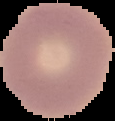

{
  "preparation": "thin blood smear",
  "image_type": "cell region segmented out of the field of view; surrounding area masked to black",
  "image_size": "115×121 pixels",
  "malaria_status": "uninfected"
}